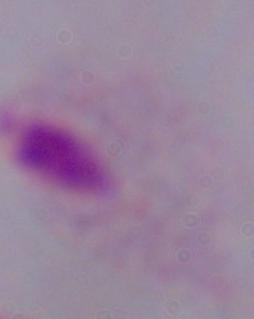

modality = micrograph
magnification = 1000x
identification = trichomonad